Report the malaria status of this cell.
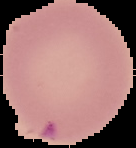
It is parasitized.

image type = segmented cell region with the area outside set to black
preparation = thin blood smear
image size = 136×148 pixels